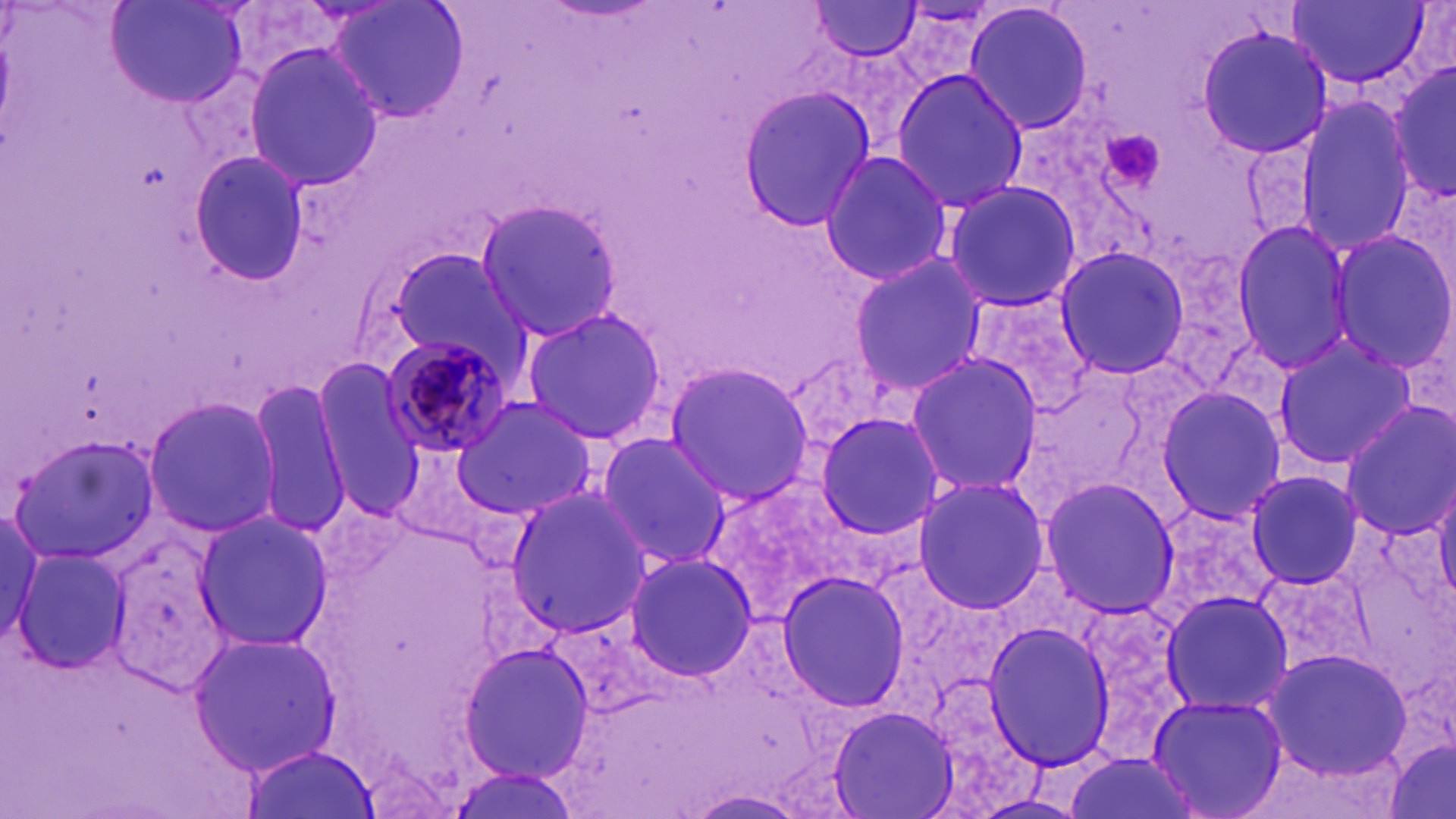

Approximate bounding boxes as (x1,y1)-(x2,y2) corner pairs in pixels. Plasmodium malariae-infected red blood cell locations: (379,334)-(519,458). Uninfected red blood cell locations: (109,0)-(248,110), (326,0)-(471,125), (1286,0)-(1429,88), (810,1)-(924,60), (963,1)-(1095,135), (1197,25)-(1332,160), (243,43)-(383,191), (1385,55)-(1455,208), (890,68)-(1029,212), (736,85)-(877,230), (1295,96)-(1421,257), (188,150)-(309,285), (818,151)-(954,286), (1381,173)-(1456,306), (939,180)-(1082,313), (474,196)-(626,344), (1228,220)-(1357,371), (1328,231)-(1456,370), (1052,245)-(1190,381), (384,249)-(526,373), (847,253)-(987,394), (962,290)-(1100,414), (519,305)-(668,447), (1268,337)-(1418,470), (903,354)-(1041,498), (312,362)-(431,516), (661,362)-(813,504), (253,378)-(354,538), (1153,386)-(1286,527), (142,394)-(281,538), (449,396)-(598,521), (1338,401)-(1456,538), (813,410)-(945,537), (593,431)-(733,569), (8,432)-(158,561), (391,441)-(502,549), (1243,469)-(1365,591), (1433,474)-(1456,604), (912,475)-(1050,613), (1037,477)-(1180,616), (502,487)-(651,635), (0,507)-(67,662), (191,512)-(335,652), (12,547)-(131,677), (623,552)-(758,681), (777,571)-(911,712), (1158,589)-(1292,715), (981,620)-(1116,772), (186,628)-(340,780), (457,640)-(593,784), (1259,646)-(1415,781), (1147,693)-(1287,819), (828,703)-(959,817), (1385,736)-(1456,819), (241,744)-(377,818), (1060,751)-(1204,819), (445,769)-(586,819), (682,791)-(811,819). Platelet locations: (1103,128)-(1166,198). Slide-level diagnosis: Plasmodium malariae. 1000x magnification. Thin blood smear. May-Grünwald-Giemsa stain. Optical microscopy. Image is 1456×819 pixels. One field of a larger specimen.